Locate and identify every blood parasite.
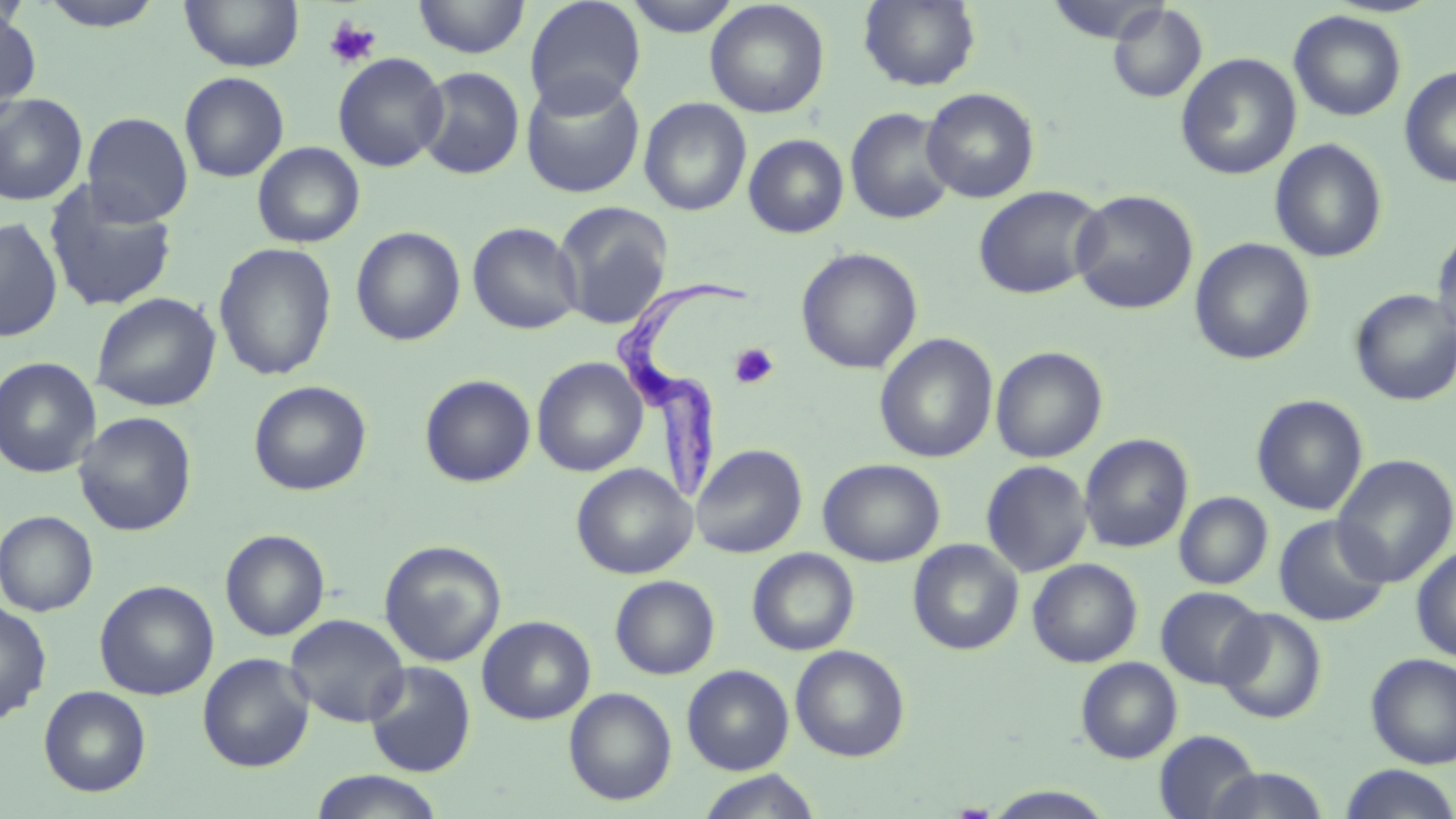
Approximate bounding boxes as (x1, y1, x2, y2) in pixels.
Trypanosoma brucei: (611, 275, 751, 503).
No Plasmodium falciparum, Plasmodium ovale, Plasmodium malariae, Plasmodium vivax, or Babesia divergens observed.

Summary:
  - Uninfected red blood cell locations: (179, 0, 304, 72), (413, 0, 531, 59), (524, 0, 646, 114), (622, 0, 744, 37), (858, 0, 982, 91), (1044, 0, 1170, 44), (33, 1, 169, 31), (705, 1, 830, 119), (1107, 3, 1207, 104), (0, 6, 41, 119), (1289, 10, 1407, 122), (332, 52, 449, 172), (1176, 53, 1301, 180), (1399, 65, 1456, 188), (415, 66, 525, 180), (179, 71, 289, 182), (521, 75, 645, 198), (921, 87, 1040, 203), (0, 93, 88, 206), (639, 98, 752, 216), (845, 107, 957, 225), (82, 112, 193, 226), (641, 120, 849, 229), (743, 134, 849, 238), (1269, 139, 1388, 262), (252, 142, 364, 248), (42, 181, 179, 312), (973, 185, 1105, 300), (1070, 189, 1199, 314), (553, 201, 674, 330), (0, 217, 63, 343), (467, 221, 584, 335), (351, 225, 466, 345), (1432, 226, 1456, 345), (1189, 238, 1315, 365), (213, 242, 338, 381), (796, 247, 923, 374), (1349, 288, 1456, 406), (91, 292, 221, 412), (874, 333, 998, 464), (991, 345, 1108, 463), (0, 356, 101, 478), (532, 357, 647, 476), (420, 374, 536, 487), (248, 380, 372, 496), (1251, 394, 1368, 516), (73, 412, 196, 536), (1079, 434, 1193, 554), (691, 443, 807, 558), (1332, 454, 1456, 587), (818, 458, 945, 566), (981, 460, 1092, 578), (571, 463, 697, 579), (1174, 492, 1273, 590), (1, 510, 99, 616), (1273, 515, 1392, 627), (220, 529, 330, 641), (378, 539, 507, 667), (908, 539, 1023, 655), (1411, 545, 1456, 662), (747, 548, 859, 656), (1027, 559, 1142, 667), (610, 575, 720, 679), (95, 579, 218, 700), (1156, 586, 1267, 689), (0, 600, 52, 726), (1216, 608, 1327, 723), (284, 613, 410, 727), (477, 615, 595, 724), (791, 645, 910, 761), (197, 652, 315, 772), (1365, 652, 1456, 768), (1076, 657, 1182, 763), (364, 661, 476, 777), (682, 665, 794, 774), (39, 686, 151, 796), (564, 687, 677, 805), (1154, 730, 1263, 819), (1338, 765, 1456, 819), (1203, 767, 1331, 819), (307, 770, 446, 819), (696, 770, 823, 819), (982, 785, 1119, 819)
  - Platelet locations: (323, 16, 382, 69), (728, 343, 779, 390)
  - Slide-level diagnosis: Trypanosoma brucei
  - Image size: 1456×819 pixels
  - Field of view: single
  - Magnification: 1000x
  - Stain: May-Grünwald-Giemsa
  - Modality: light microscopy
  - Preparation: thin blood smear